State the preparation type.
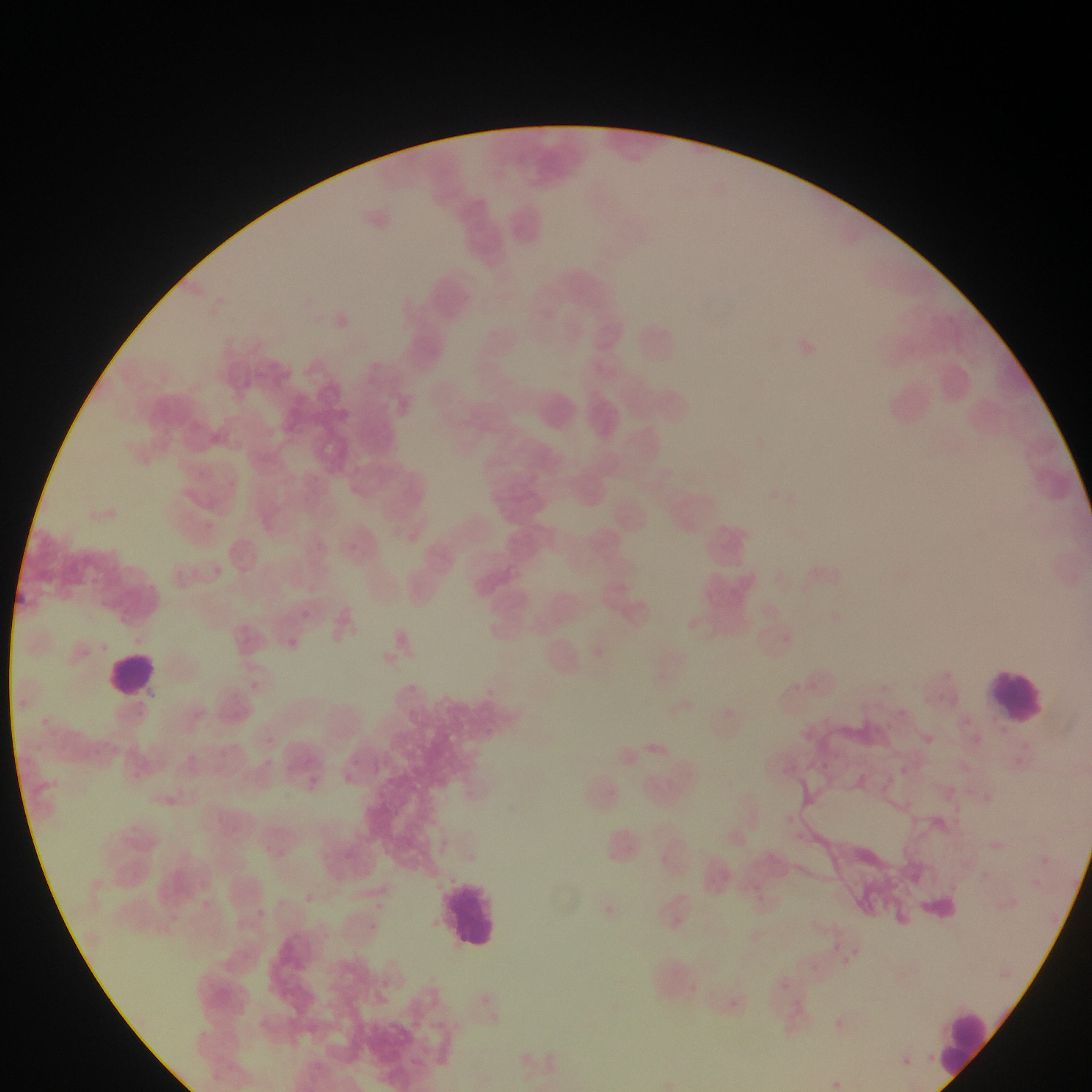
This is a thin smear.

country = Ghana
leukocyte locations = approximate bounding boxes as {left, top, right, bottom} in pixels: {627, 316, 687, 369}, {530, 386, 585, 440}, {103, 650, 160, 699}, {984, 662, 1054, 732}, {439, 871, 505, 957}, {933, 1005, 995, 1080}
field of view = single
Plasmodium parasite locations = approximate bounding boxes as {left, top, right, bottom} in pixels: {945, 670, 953, 676}, {922, 692, 930, 704}, {936, 693, 945, 703}, {950, 693, 958, 703}, {893, 706, 910, 719}, {965, 715, 975, 725}, {881, 720, 897, 732}, {484, 727, 504, 739}, {923, 735, 935, 747}, {1022, 741, 1040, 753}, {819, 760, 830, 769}, {942, 785, 960, 791}, {983, 787, 991, 800}, {953, 803, 965, 811}, {955, 810, 963, 822}, {786, 811, 805, 824}, {794, 831, 814, 847}, {1042, 851, 1054, 865}, {978, 867, 995, 874}, {1033, 875, 1042, 888}, {748, 879, 760, 896}, {947, 882, 955, 889}, {1011, 898, 1016, 907}, {827, 938, 851, 960}, {829, 938, 845, 953}, {774, 975, 793, 994}, {725, 996, 742, 1013}, {827, 1014, 851, 1038}, {824, 1076, 845, 1092} | approximate {x, y} pixel centers of objects too small to bound: {904, 769}
image size = 1092×1092 pixels
capture = mobile-phone photograph through a microscope